State the blood parasite species.
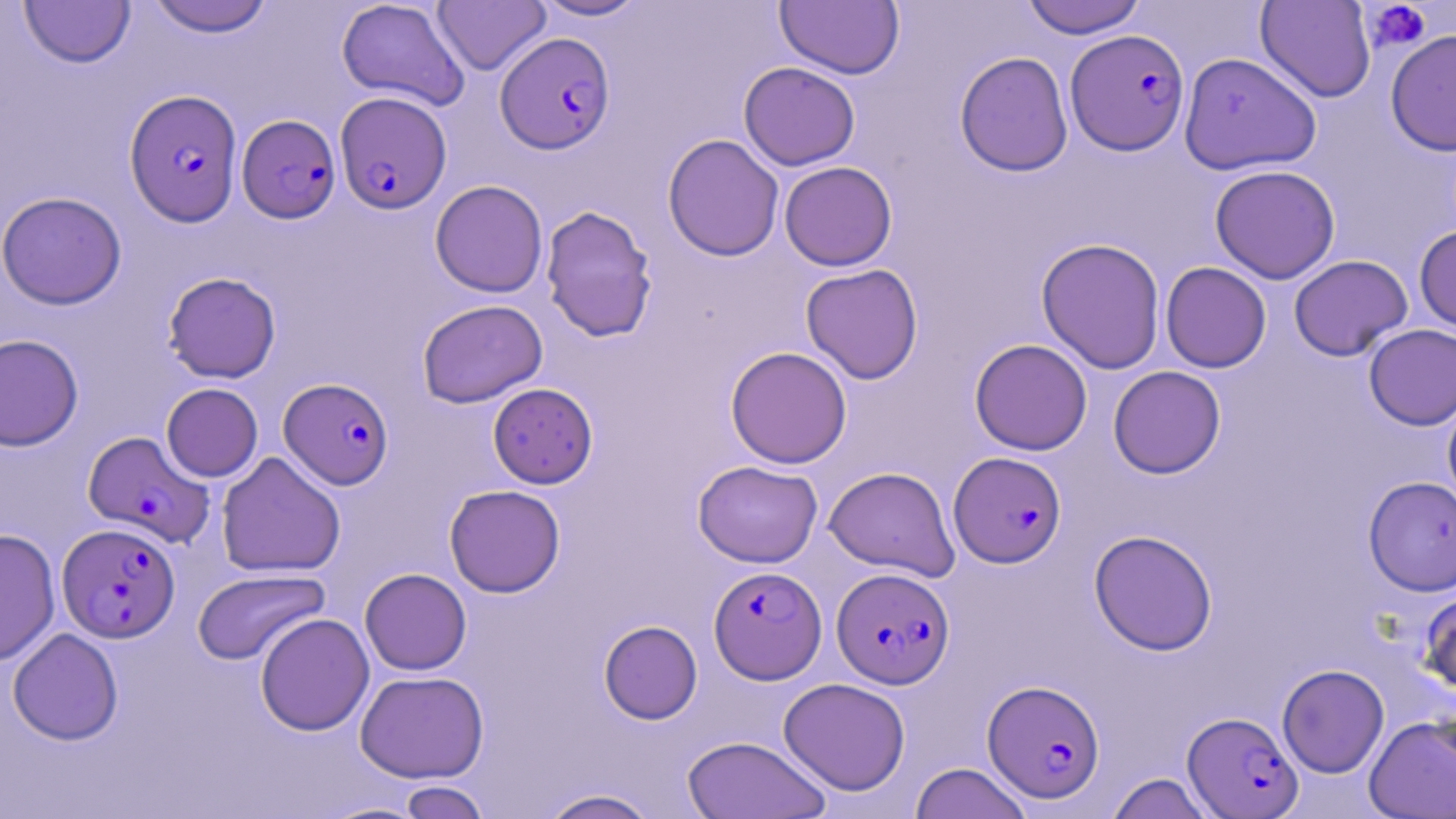
Plasmodium falciparum.

{
  "uninfected_red_blood_cell_locations": "approximate bounding boxes as (x1,y1)-(x2,y2) corner pairs in pixels: (145,0)-(275,37), (336,0)-(470,111), (431,0)-(551,75), (531,0)-(649,21), (1020,0)-(1147,39), (1255,0)-(1377,103), (18,1)-(136,68), (775,1)-(904,79), (1385,29)-(1456,156), (955,50)-(1073,177), (1178,52)-(1321,175), (738,62)-(860,170), (662,134)-(784,261), (779,161)-(897,271), (1210,165)-(1340,284), (430,180)-(548,297), (0,191)-(126,309), (541,205)-(658,341), (1414,225)-(1456,336), (1036,237)-(1166,374), (1289,254)-(1413,361), (1160,262)-(1271,373), (800,263)-(923,384), (163,271)-(281,383), (417,299)-(548,408), (1363,324)-(1456,429), (0,333)-(84,451), (969,338)-(1092,455), (725,346)-(852,468), (1108,365)-(1226,479), (161,382)-(263,482), (487,383)-(598,488), (1442,393)-(1456,509), (216,451)-(346,578), (693,460)-(823,568), (824,466)-(960,581), (1363,476)-(1456,596), (444,484)-(565,597), (0,528)-(60,666), (1089,529)-(1218,655), (192,568)-(330,666), (360,568)-(472,675), (1419,586)-(1456,700), (255,613)-(375,736), (598,620)-(702,724), (8,628)-(123,745), (1277,664)-(1389,778), (355,670)-(489,783), (779,678)-(910,795), (1364,714)-(1456,818), (682,736)-(831,819), (910,762)-(1033,819), (1107,772)-(1216,819), (397,781)-(490,819), (539,788)-(661,818), (319,800)-(431,818)",
  "stain": "May-Grünwald-Giemsa",
  "plasmodium_falciparum_infected_red_blood_cell_locations": "approximate bounding boxes as (x1,y1)-(x2,y2) corner pairs in pixels: (1065,29)-(1190,155), (494,32)-(615,154), (125,89)-(242,227), (335,91)-(451,214), (237,114)-(340,223), (279,377)-(394,489), (83,430)-(214,546), (949,451)-(1066,568), (57,523)-(181,642), (708,565)-(826,683), (832,567)-(955,688), (981,679)-(1106,803), (1182,711)-(1303,817)",
  "platelet_locations": "approximate bounding boxes as (x1,y1)-(x2,y2) corner pairs in pixels: (1362,1)-(1431,54)",
  "preparation": "thin blood film",
  "magnification": "1000x",
  "field_of_view": "single",
  "image_size": "1456×819 pixels",
  "modality": "optical microscopy"
}